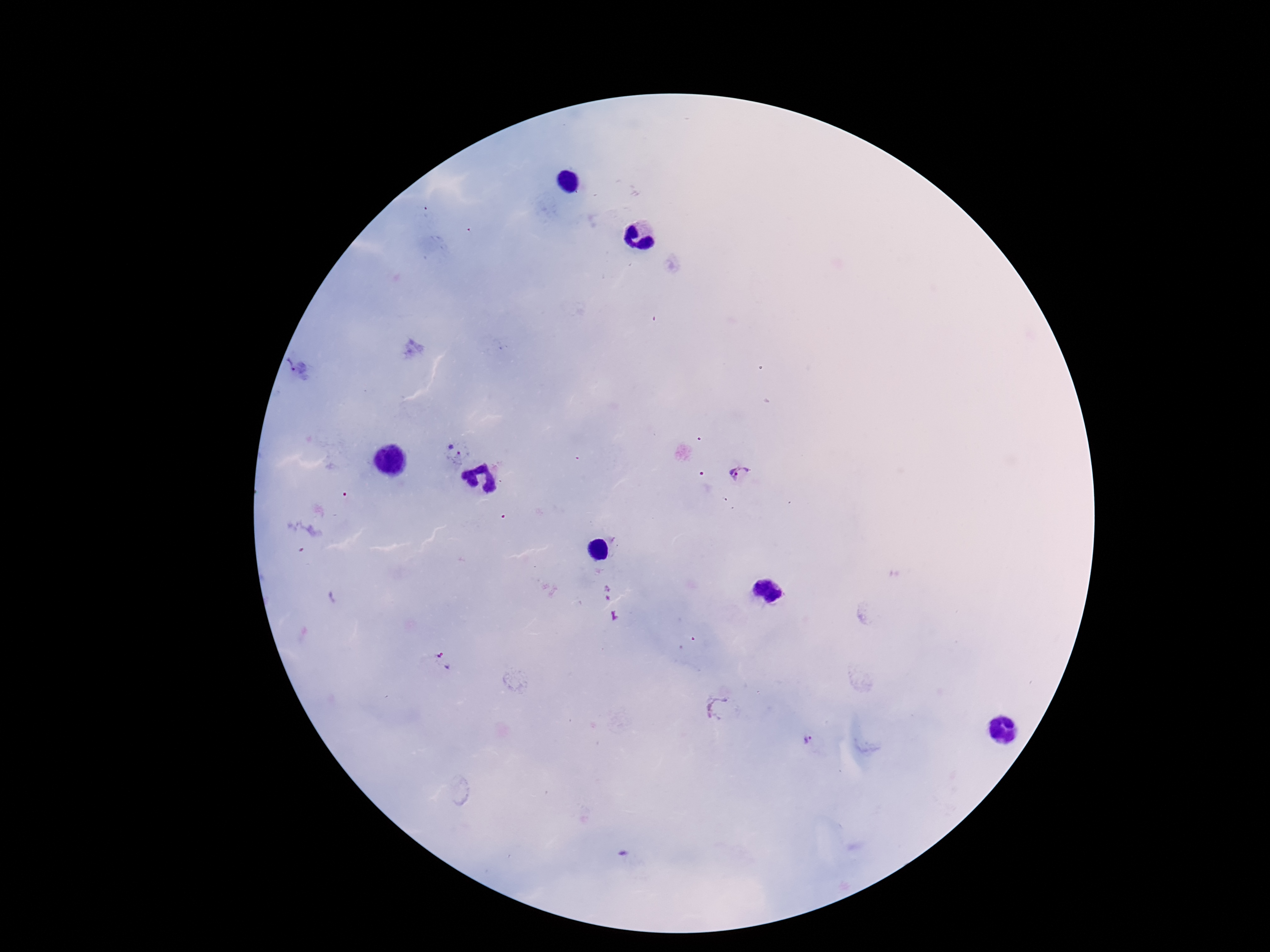
{
  "field_of_view": "single",
  "image_size": "1270×952 pixels",
  "magnification": "100x",
  "stain": "Giemsa",
  "preparation": "thick blood smear",
  "capture": "smartphone camera through the microscope eyepiece",
  "plasmodium_parasite_locations": "approximate centers as (x, y) in pixels: (290, 363), (454, 455), (739, 472), (444, 662), (808, 742)",
  "patient_malaria_status": "infected"
}